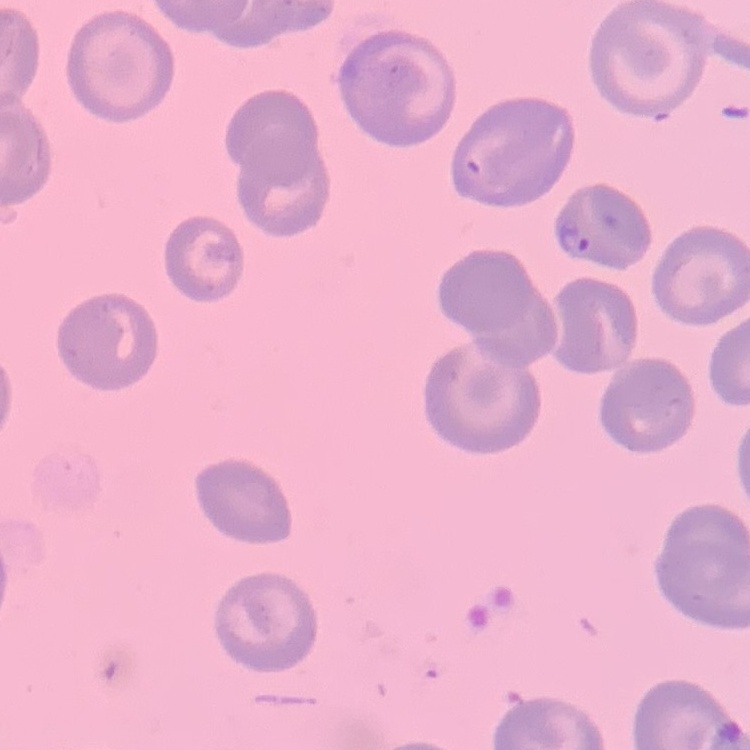

red blood cell morphology = no rouleaux formation
stain = Field's or Giemsa
image type = one tile cut from a larger photomicrograph
preparation = thin peripheral smear